Describe the morphology of the erythrocytes.
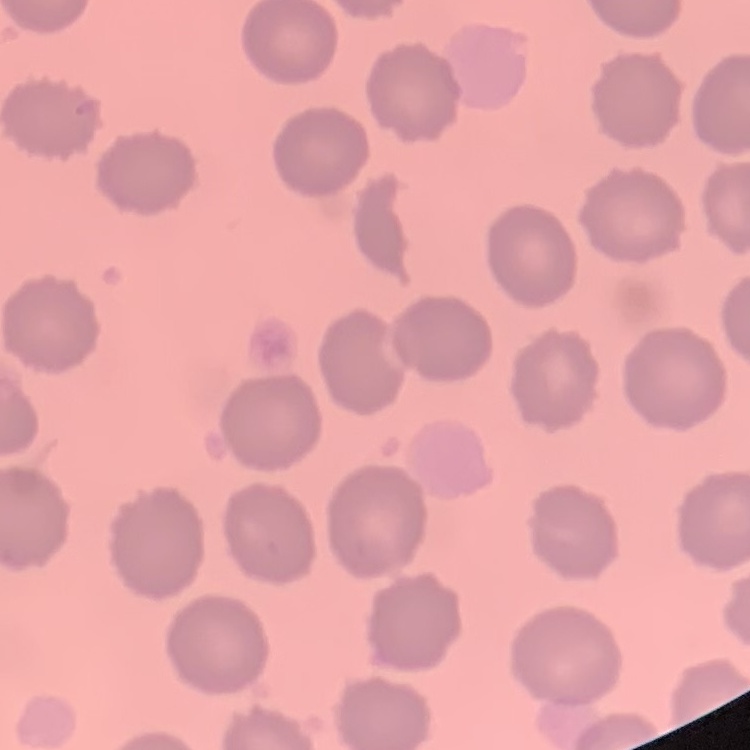
No rouleaux formation.

Field's or Giemsa stain. One tile cut from a larger photomicrograph. Thin blood smear.